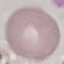
Malaria status: uninfected. Thin smear of blood. Automatically extracted cell patch, resized to 64 × 64 pixels. Giemsa stain. Photographed with a smartphone camera at the microscope eyepiece.